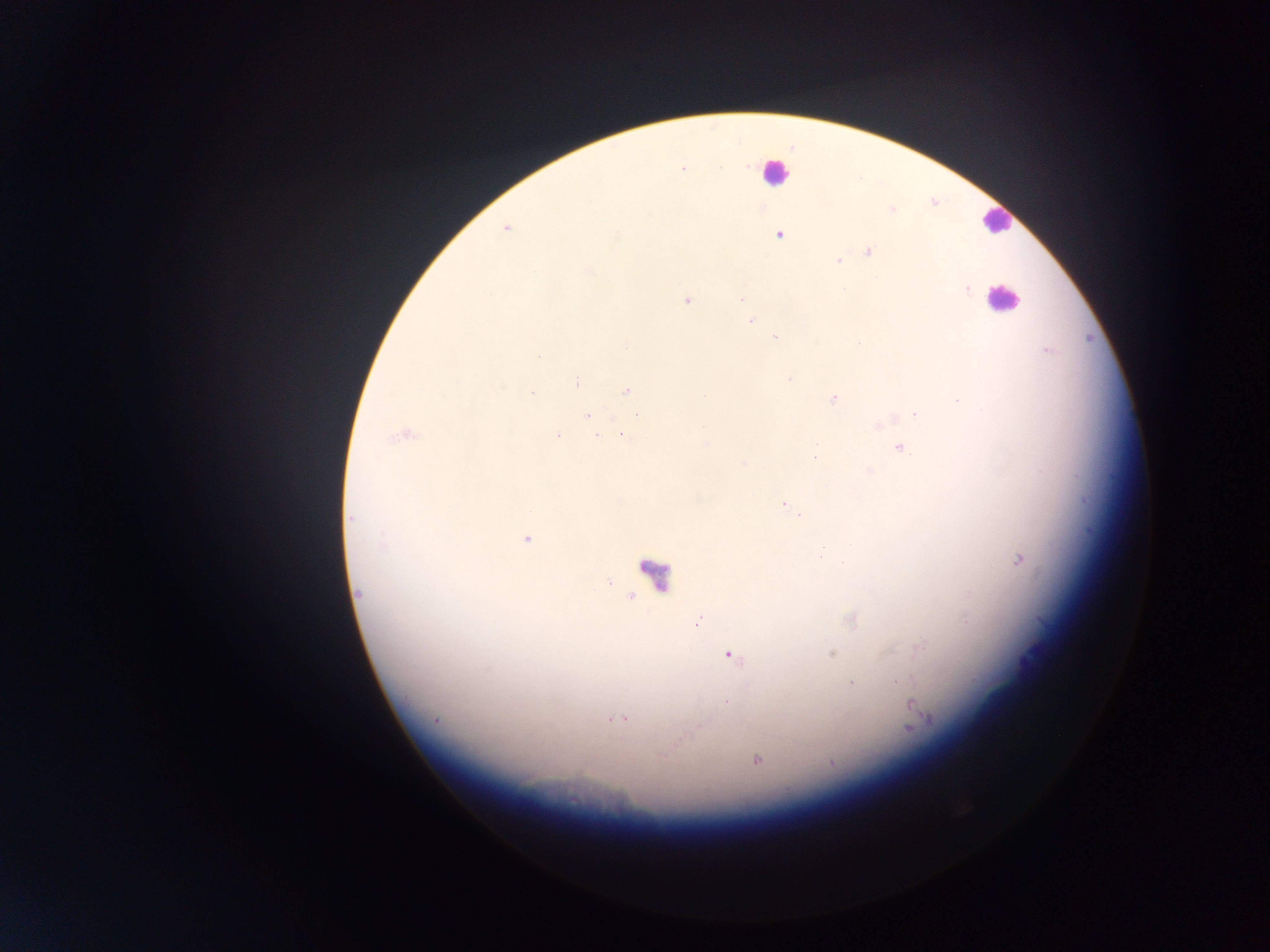 Approximate centers as [x, y] in pixels. Leukocyte locations: [775, 171], [996, 220], [1001, 299], [651, 572]. Plasmodium parasite locations: [892, 211], [506, 227], [780, 233], [868, 250], [838, 260], [966, 289], [742, 297], [687, 300], [751, 320], [775, 338], [1046, 350], [577, 382], [627, 391], [833, 398], [916, 414], [588, 415], [623, 433], [404, 434], [557, 435], [899, 446], [783, 503], [350, 519], [527, 539], [1019, 559], [358, 594], [630, 596], [698, 619], [851, 620], [727, 653], [831, 653], [852, 684], [726, 702], [913, 709], [616, 718], [756, 759], [831, 764]. Thick blood smear. One field of view. Photographed through a microscope with a mobile-phone camera. Image is 1270×952 pixels. Sample from Ghana.